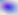

identification = Toxoplasma gondii
magnification = 400x
modality = micrograph